Classify this cell by malaria status.
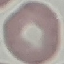
It is uninfected.

Thin blood film. Giemsa-stained preparation. Cell patch, automatically extracted from a larger field of view and resized to 64 × 64 pixels. Photographed with a smartphone camera at the microscope eyepiece.